Locate platelets.
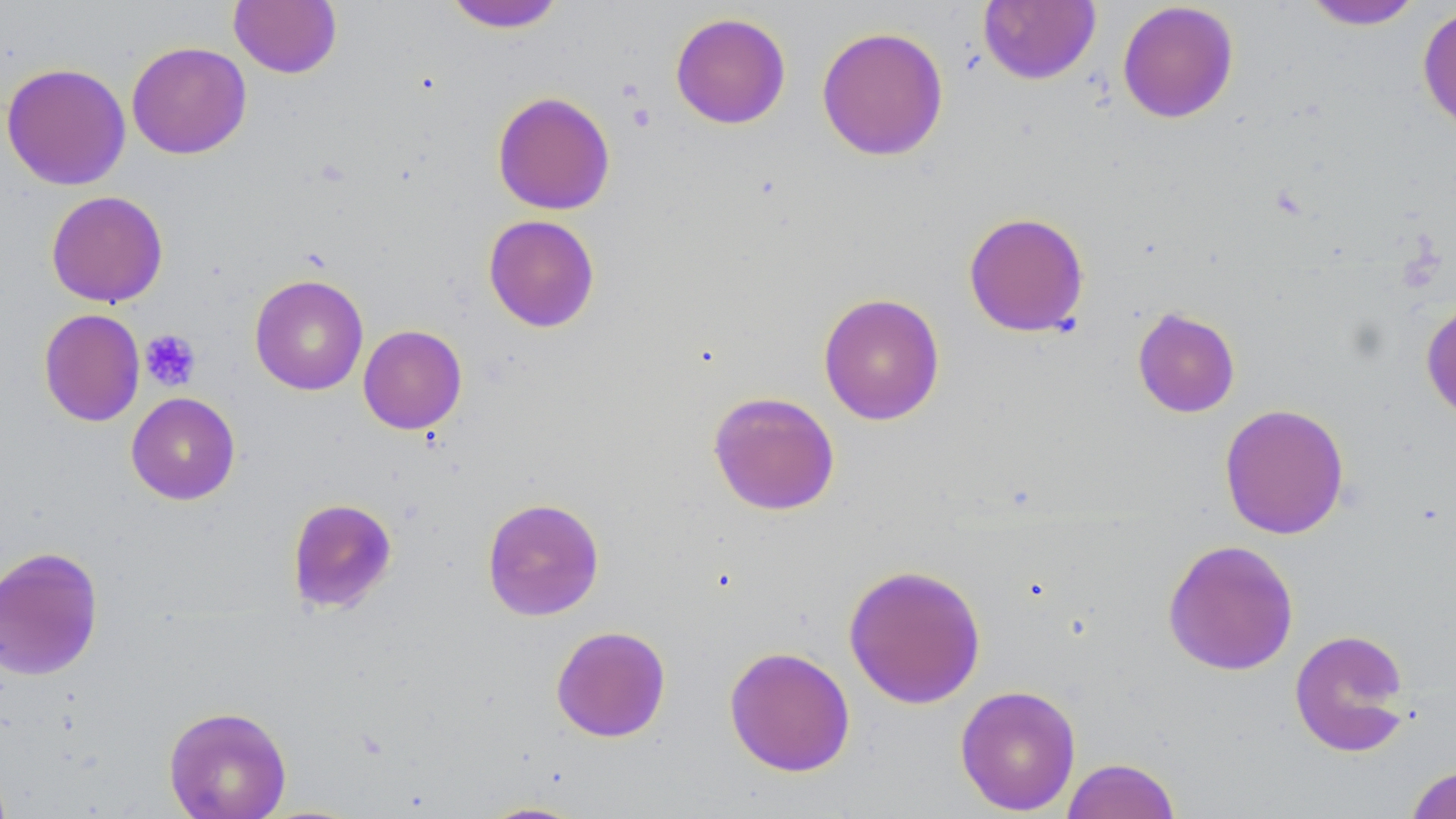
Approximate bounding boxes as (x1, y1, x2, y2) in pixels.
Platelets: (627, 102, 656, 131), (140, 329, 201, 391).

Summary:
  - Uninfected red blood cell locations: (442, 0, 567, 33), (977, 0, 1101, 86), (229, 1, 342, 79), (1300, 1, 1426, 31), (1117, 2, 1240, 123), (1416, 4, 1456, 136), (670, 12, 791, 129), (816, 25, 949, 161), (126, 41, 252, 159), (1, 62, 131, 190), (491, 91, 616, 216), (46, 190, 168, 308), (963, 211, 1090, 337), (483, 214, 600, 333), (249, 274, 369, 396), (818, 292, 945, 425), (1420, 299, 1456, 422), (1132, 307, 1240, 418), (38, 308, 145, 427), (357, 324, 467, 434), (707, 391, 841, 516), (126, 392, 241, 505), (1219, 403, 1350, 540), (286, 497, 398, 614), (481, 497, 605, 621), (1162, 539, 1299, 676), (0, 546, 104, 681), (843, 563, 987, 709), (551, 625, 671, 742), (1289, 629, 1412, 756), (723, 646, 856, 777), (955, 684, 1081, 815), (163, 705, 292, 819), (1061, 757, 1180, 818), (1405, 763, 1456, 819), (475, 800, 592, 818)
  - Slide-level diagnosis: no evidence of blood parasites
  - Preparation: thin blood film
  - Image size: 1456×819 pixels
  - Stain: May-Grünwald-Giemsa
  - Field of view: single
  - Magnification: 1000x
  - Modality: optical microscopy